Identify the parasite.
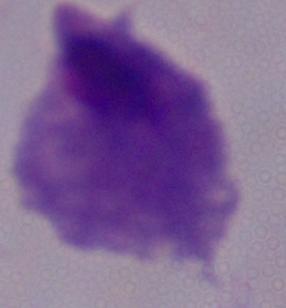
This is a trichomonad.

magnification = 1000x
modality = photomicrograph